Describe the morphology of the erythrocytes.
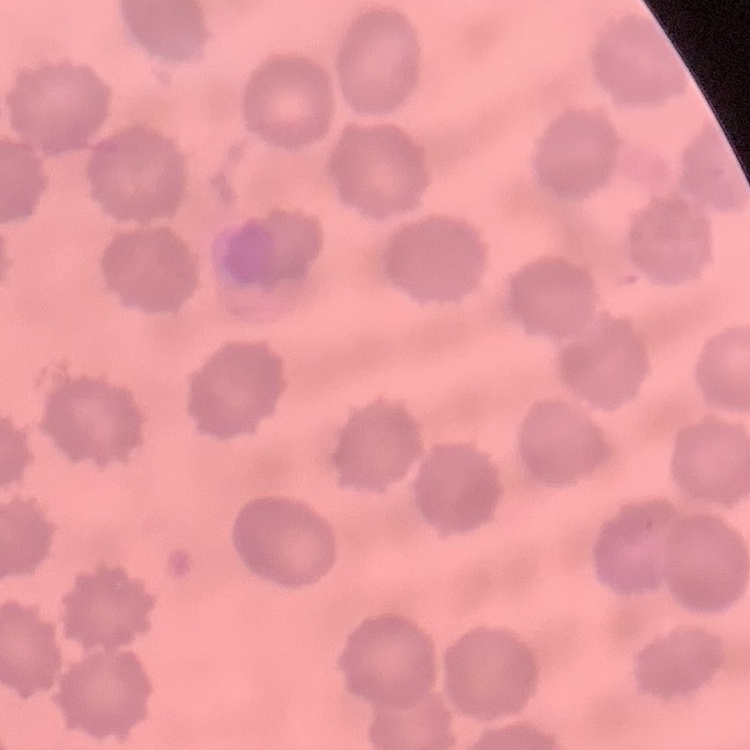
They show no rouleaux formation.

Summary:
  - Image type: square crop of a larger photomicrograph
  - Stain: Field's or Giemsa
  - Preparation: thin blood smear